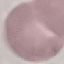
{
  "result": "no malaria parasites seen",
  "preparation": "thin blood film",
  "capture": "smartphone camera at the microscope eyepiece",
  "image_type": "cell patch, automatically extracted from a larger field of view and resized to 64 × 64 pixels",
  "stain": "Giemsa"
}